Locate every malaria parasite and every leukocyte.
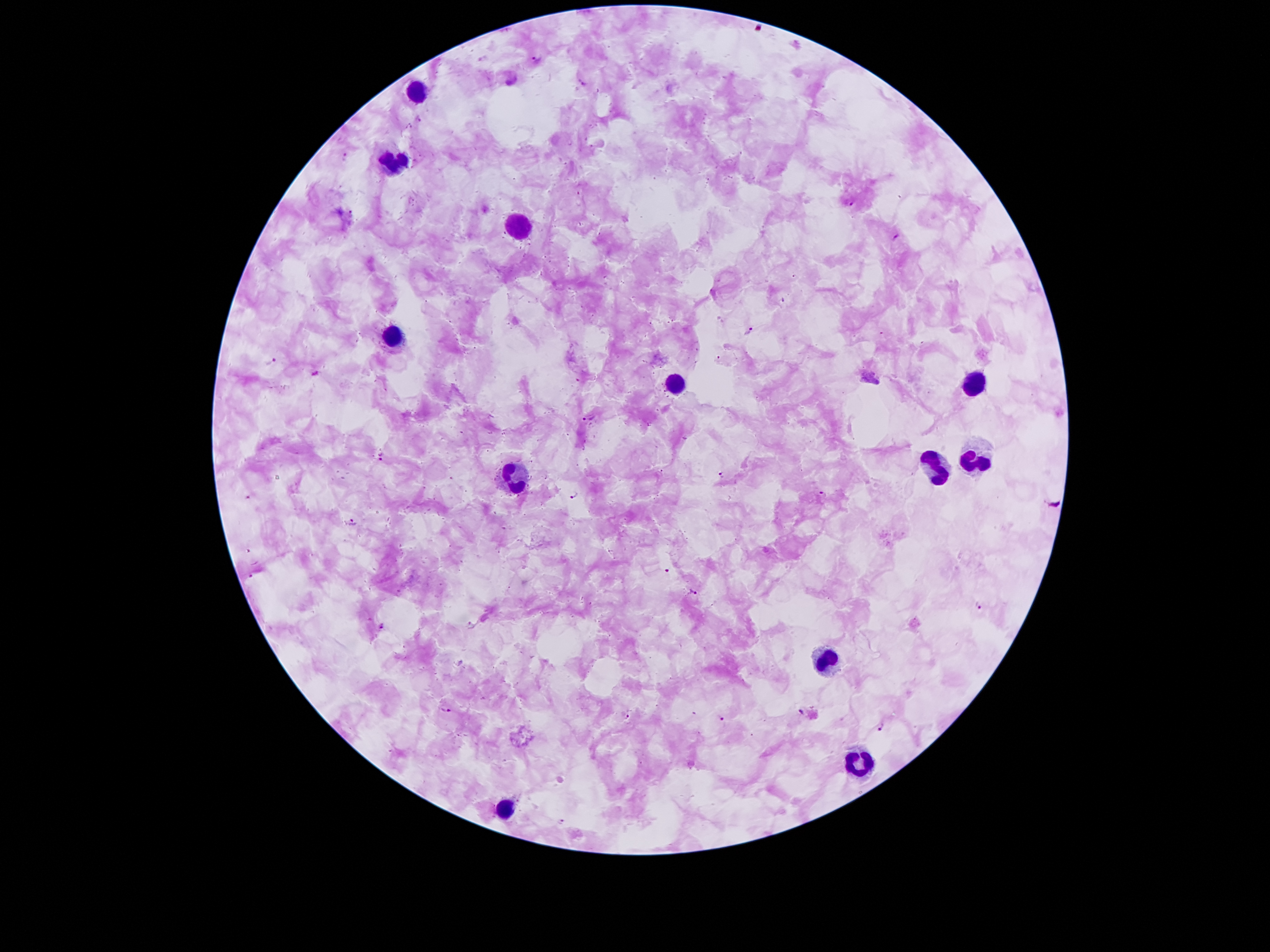

Approximate centers as (x, y) in pixels.
Malaria parasites: (535, 56), (582, 84), (418, 120), (345, 158), (577, 195), (852, 204), (351, 213), (896, 237), (783, 301), (750, 330), (272, 361), (591, 418), (380, 457), (721, 474), (575, 496), (822, 496), (350, 521), (667, 571), (251, 576), (693, 593), (978, 606), (383, 627), (445, 708), (801, 711), (626, 715), (723, 719), (881, 727), (562, 822).
Leukocytes: (413, 90), (393, 165), (513, 227), (393, 339), (676, 381), (973, 383), (973, 458), (931, 470), (513, 479), (830, 665), (855, 759), (508, 808).

capture: smartphone through the microscope eyepiece
patient_malaria_status: positive for Plasmodium falciparum
stain: Giemsa
preparation: thick blood film
field_of_view: single
magnification: 100x
image_size: 1270×952 pixels